Identify the blood parasite species.
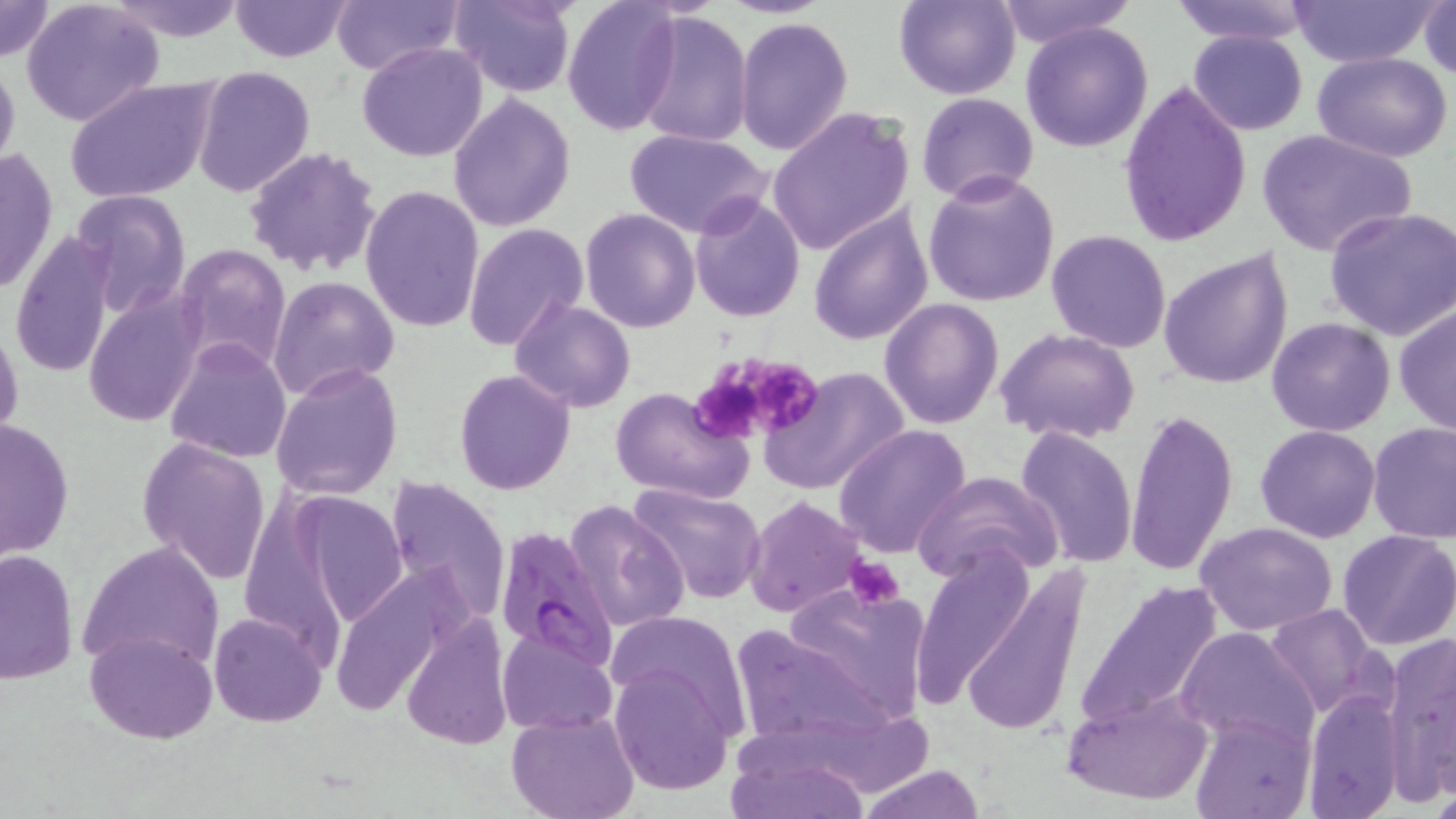
Plasmodium falciparum.

Approximate bounding boxes as named x1/y1/x2/y2 corners in pixels. Plasmodium falciparum-infected red blood cell locations: (x1=492, y1=527, x2=616, y2=673). Uninfected red blood cell locations: (x1=0, y1=0, x2=55, y2=63), (x1=230, y1=0, x2=354, y2=62), (x1=328, y1=0, x2=464, y2=76), (x1=453, y1=0, x2=576, y2=98), (x1=561, y1=0, x2=682, y2=136), (x1=895, y1=0, x2=1020, y2=100), (x1=995, y1=0, x2=1134, y2=48), (x1=1168, y1=0, x2=1319, y2=47), (x1=1290, y1=0, x2=1441, y2=68), (x1=21, y1=1, x2=165, y2=127), (x1=104, y1=2, x2=250, y2=43), (x1=1420, y1=2, x2=1455, y2=80), (x1=634, y1=11, x2=752, y2=149), (x1=735, y1=16, x2=854, y2=156), (x1=1020, y1=20, x2=1154, y2=154), (x1=1187, y1=30, x2=1309, y2=135), (x1=356, y1=41, x2=488, y2=163), (x1=1312, y1=52, x2=1454, y2=163), (x1=0, y1=55, x2=20, y2=179), (x1=191, y1=66, x2=314, y2=197), (x1=66, y1=77, x2=218, y2=203), (x1=1119, y1=79, x2=1251, y2=248), (x1=917, y1=92, x2=1038, y2=202), (x1=447, y1=93, x2=576, y2=232), (x1=767, y1=106, x2=915, y2=255), (x1=1255, y1=127, x2=1418, y2=261), (x1=625, y1=129, x2=772, y2=238), (x1=1, y1=145, x2=58, y2=300), (x1=243, y1=147, x2=384, y2=279), (x1=923, y1=170, x2=1060, y2=307), (x1=362, y1=185, x2=486, y2=333), (x1=71, y1=189, x2=191, y2=316), (x1=689, y1=190, x2=807, y2=321), (x1=807, y1=201, x2=933, y2=347), (x1=1323, y1=206, x2=1456, y2=341), (x1=580, y1=208, x2=701, y2=332), (x1=462, y1=223, x2=587, y2=354), (x1=1046, y1=229, x2=1172, y2=352), (x1=9, y1=232, x2=117, y2=382), (x1=172, y1=244, x2=291, y2=375), (x1=1157, y1=249, x2=1295, y2=391), (x1=267, y1=276, x2=399, y2=401), (x1=82, y1=288, x2=206, y2=427), (x1=509, y1=296, x2=635, y2=412), (x1=879, y1=297, x2=1004, y2=430), (x1=1393, y1=303, x2=1456, y2=438), (x1=1266, y1=317, x2=1394, y2=437), (x1=0, y1=319, x2=24, y2=452), (x1=995, y1=327, x2=1141, y2=445), (x1=163, y1=339, x2=293, y2=463), (x1=272, y1=361, x2=403, y2=502), (x1=761, y1=366, x2=910, y2=495), (x1=454, y1=370, x2=575, y2=495), (x1=608, y1=386, x2=754, y2=504), (x1=1125, y1=408, x2=1239, y2=576), (x1=0, y1=415, x2=74, y2=563), (x1=1366, y1=422, x2=1456, y2=545), (x1=833, y1=425, x2=970, y2=558), (x1=1255, y1=425, x2=1381, y2=543), (x1=1014, y1=426, x2=1139, y2=568), (x1=136, y1=437, x2=271, y2=584), (x1=912, y1=470, x2=1064, y2=583), (x1=384, y1=476, x2=510, y2=626), (x1=626, y1=482, x2=768, y2=604), (x1=290, y1=490, x2=408, y2=630), (x1=744, y1=497, x2=866, y2=619), (x1=565, y1=500, x2=688, y2=633), (x1=1195, y1=520, x2=1338, y2=637), (x1=1337, y1=529, x2=1456, y2=649), (x1=77, y1=539, x2=226, y2=673), (x1=913, y1=545, x2=1037, y2=709), (x1=0, y1=547, x2=78, y2=687), (x1=958, y1=564, x2=1092, y2=739), (x1=325, y1=566, x2=468, y2=720), (x1=1073, y1=576, x2=1225, y2=731), (x1=783, y1=580, x2=932, y2=723), (x1=1263, y1=603, x2=1388, y2=719), (x1=210, y1=611, x2=327, y2=726), (x1=401, y1=614, x2=517, y2=750), (x1=607, y1=614, x2=752, y2=733), (x1=727, y1=624, x2=891, y2=751), (x1=1174, y1=625, x2=1319, y2=746), (x1=85, y1=628, x2=217, y2=743), (x1=496, y1=629, x2=616, y2=734), (x1=1382, y1=630, x2=1456, y2=802), (x1=608, y1=658, x2=736, y2=796), (x1=1062, y1=686, x2=1213, y2=806), (x1=1302, y1=687, x2=1402, y2=819), (x1=505, y1=709, x2=641, y2=819), (x1=1190, y1=710, x2=1313, y2=819), (x1=723, y1=741, x2=871, y2=818), (x1=858, y1=763, x2=983, y2=819). Platelet locations: (x1=691, y1=351, x2=819, y2=444), (x1=844, y1=554, x2=906, y2=612). One field of a larger specimen. Captured at 1000x magnification. May-Grünwald-Giemsa stain. Optical microscopy. Image is 1456×819 pixels. Thin blood film.